Comment on the morphology of the erythrocytes.
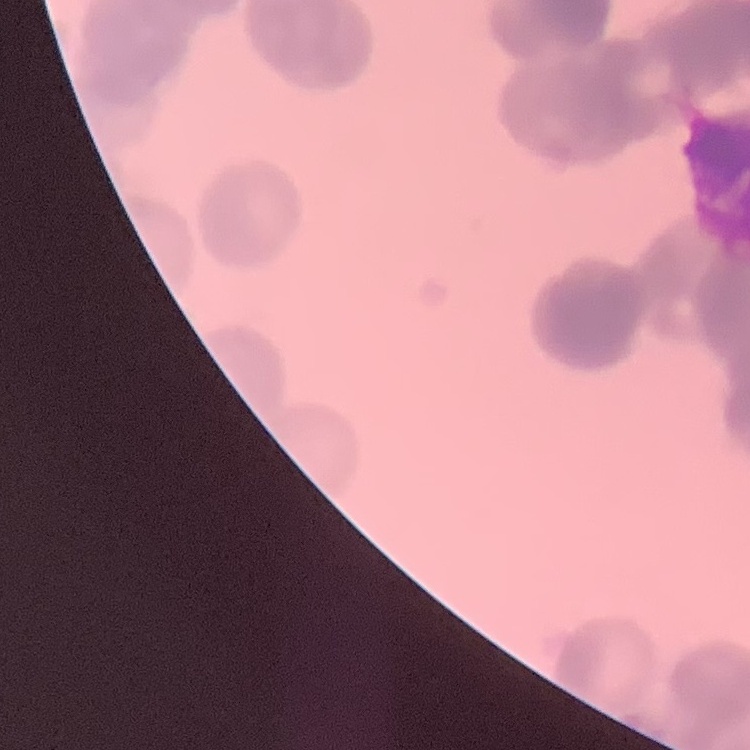

They show rouleaux formation.

Thin blood film. Stained with either Field's or Giemsa. Square crop of a larger photomicrograph.